Classify this cell by malaria status.
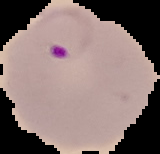

It is parasitized.

From a thin blood film. Cell region segmented out of the field of view; the surrounding area is masked to black. Image is 160×154 pixels.